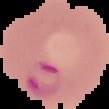

Summary:
  - Malaria status: parasitized
  - Preparation: thin blood film
  - Image size: 109×109 pixels
  - Image type: cell region segmented out of the field of view; surrounding area masked to black